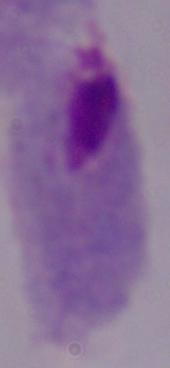

Micrograph. A trichomonad is shown. Captured at 1000x magnification.